Classify this cell by malaria status.
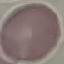

Uninfected.

Summary:
  - Preparation: thin blood film
  - Capture: smartphone camera at the microscope eyepiece
  - Image type: cell patch, automatically extracted from a larger field of view and resized to 64 × 64 pixels
  - Stain: Giemsa